Assess this cell for malaria.
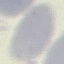
It is uninfected.

Cell patch, automatically extracted from a larger field of view and resized to 64 × 64 pixels. Thin blood smear. Giemsa stain. Acquired by smartphone through the microscope eyepiece.